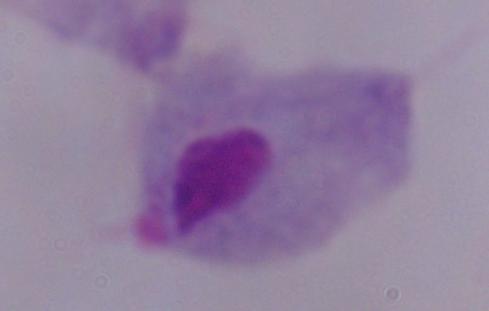

Summary:
  - Identification: trichomonad
  - Magnification: 1000x
  - Modality: micrograph